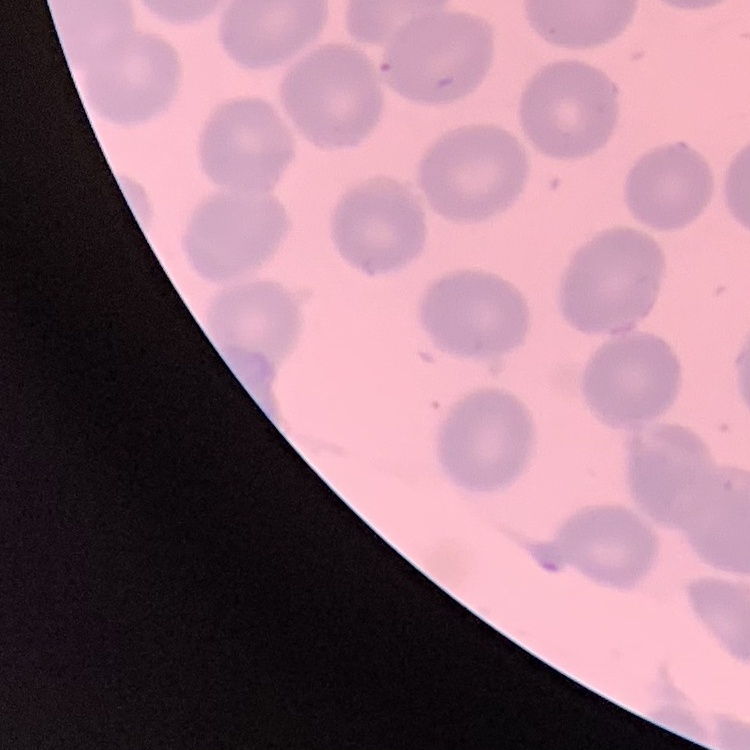
The erythrocytes exhibit no rouleaux formation. Thin peripheral smear. Field's or Giemsa stain. Square crop of a larger photomicrograph.